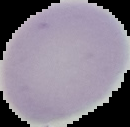
Summary:
  - Image type: cell region segmented out of the field of view; surrounding area masked to black
  - Malaria status: uninfected
  - Image size: 130×127 pixels
  - Preparation: thin blood smear